Describe the morphology of the erythrocytes.
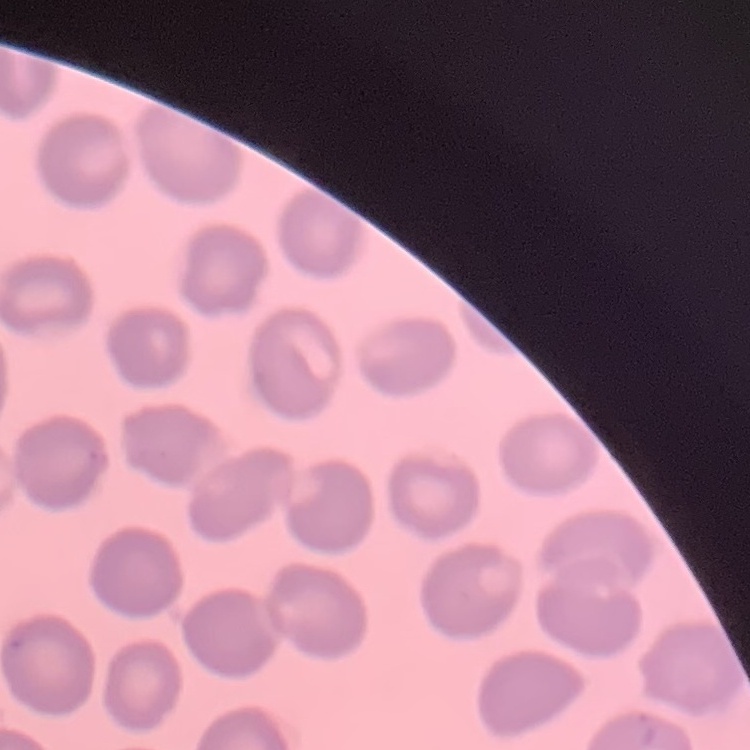
No rouleaux formation.

Square crop of a larger photomicrograph. Field's or Giemsa stain. Thin blood film.